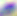

400x magnification. Photomicrograph. Toxoplasma gondii is shown.